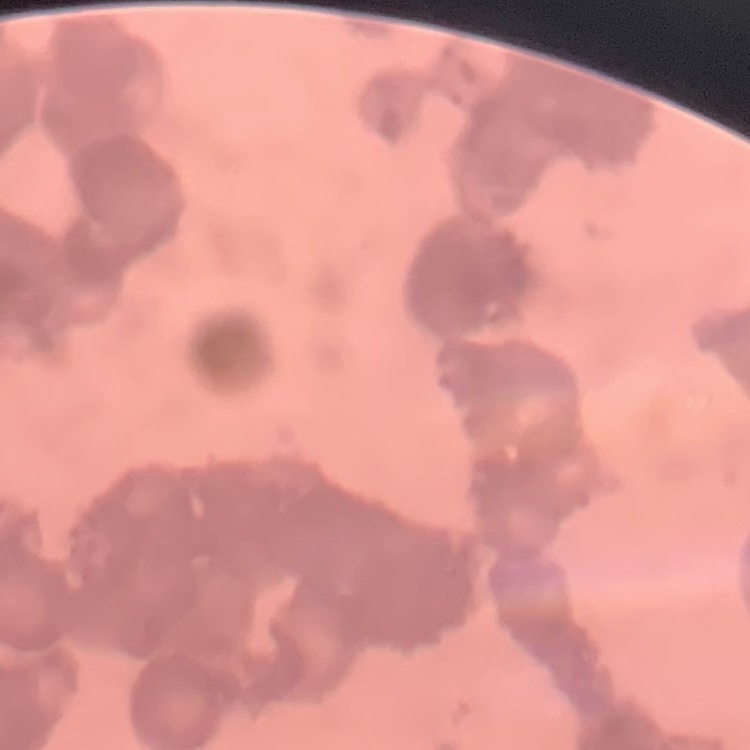
The red blood cells exhibit rouleaux formation. Thin blood film. Stained with either Field's or Giemsa. One tile cut from a larger photomicrograph.